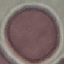 Result: no malaria parasites seen. Thin smear of blood. Giemsa-stained preparation. Acquired by smartphone through the microscope eyepiece. Automatically extracted cell patch, resized to 64 × 64 pixels.